Locate every Babesia divergens-infected red blood cell.
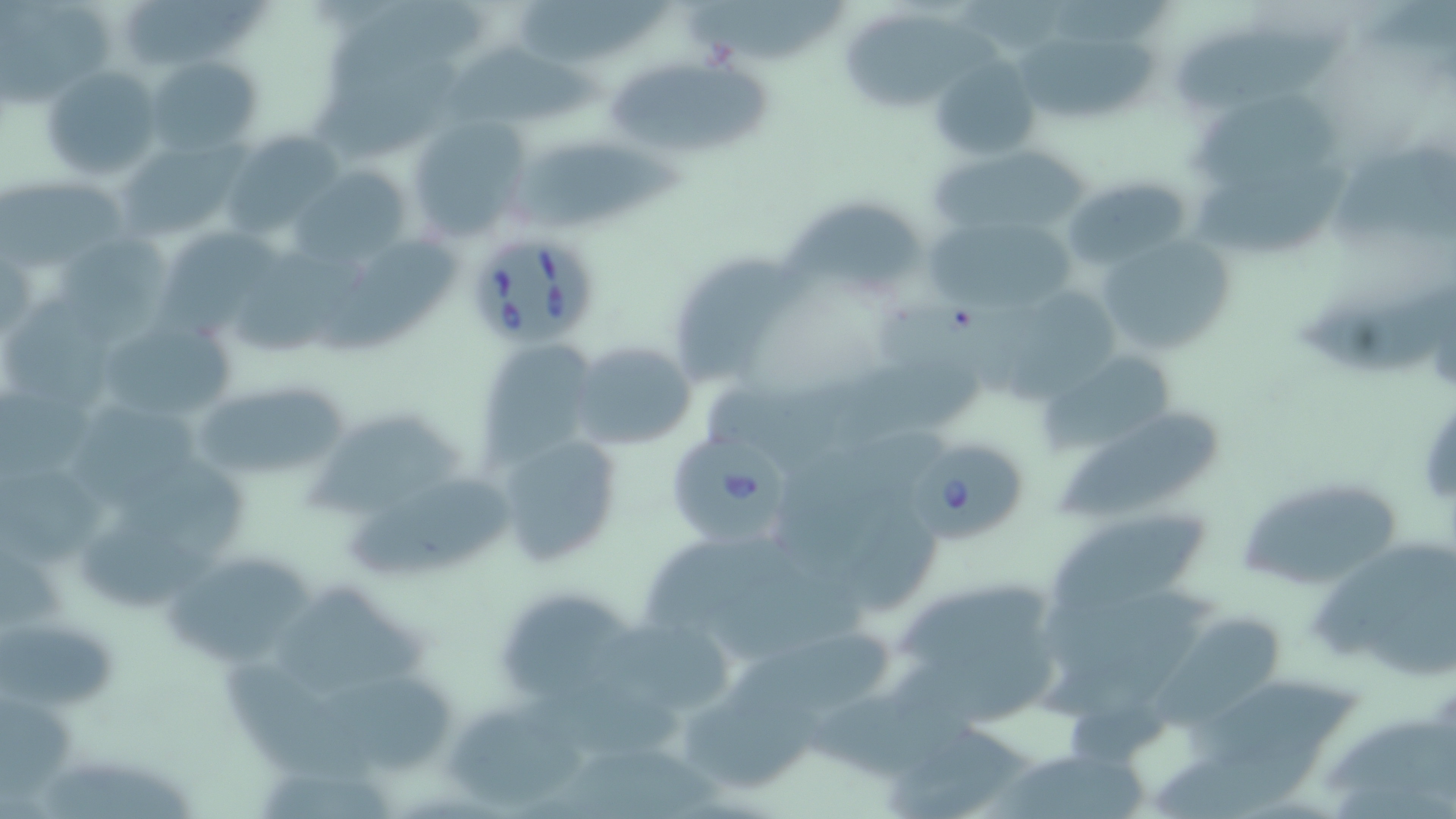
Approximate bounding boxes as named x1/y1/x2/y2 corners in pixels.
Babesia divergens-infected red blood cells: (x1=465, y1=230, x2=597, y2=346), (x1=672, y1=431, x2=793, y2=544), (x1=910, y1=436, x2=1029, y2=546).

Uninfected red blood cell locations: (x1=1, y1=0, x2=122, y2=107), (x1=129, y1=0, x2=273, y2=59), (x1=685, y1=0, x2=847, y2=72), (x1=519, y1=1, x2=672, y2=66), (x1=847, y1=13, x2=1007, y2=111), (x1=1174, y1=27, x2=1350, y2=109), (x1=1023, y1=35, x2=1161, y2=118), (x1=444, y1=45, x2=618, y2=134), (x1=312, y1=54, x2=468, y2=158), (x1=149, y1=55, x2=259, y2=156), (x1=931, y1=56, x2=1041, y2=160), (x1=605, y1=60, x2=779, y2=155), (x1=43, y1=66, x2=163, y2=182), (x1=1193, y1=92, x2=1345, y2=189), (x1=404, y1=117, x2=530, y2=243), (x1=227, y1=139, x2=344, y2=243), (x1=117, y1=141, x2=240, y2=243), (x1=508, y1=143, x2=689, y2=240), (x1=933, y1=146, x2=1088, y2=244), (x1=1337, y1=147, x2=1455, y2=241), (x1=1195, y1=166, x2=1350, y2=256), (x1=287, y1=167, x2=410, y2=269), (x1=1061, y1=174, x2=1194, y2=272), (x1=1, y1=179, x2=135, y2=268), (x1=783, y1=200, x2=932, y2=296), (x1=917, y1=220, x2=1083, y2=311), (x1=165, y1=228, x2=290, y2=331), (x1=1093, y1=231, x2=1239, y2=359), (x1=56, y1=232, x2=176, y2=339), (x1=322, y1=236, x2=461, y2=357), (x1=236, y1=246, x2=363, y2=358), (x1=674, y1=252, x2=806, y2=377), (x1=1294, y1=280, x2=1455, y2=375), (x1=881, y1=284, x2=1036, y2=402), (x1=999, y1=287, x2=1119, y2=406), (x1=1, y1=300, x2=131, y2=413), (x1=101, y1=317, x2=240, y2=427), (x1=476, y1=339, x2=598, y2=468), (x1=569, y1=341, x2=699, y2=450), (x1=1046, y1=350, x2=1180, y2=457), (x1=197, y1=385, x2=355, y2=472), (x1=78, y1=402, x2=208, y2=511), (x1=1063, y1=409, x2=1225, y2=516), (x1=303, y1=411, x2=475, y2=516), (x1=782, y1=420, x2=962, y2=568), (x1=490, y1=429, x2=623, y2=565), (x1=1, y1=468, x2=111, y2=570), (x1=114, y1=468, x2=251, y2=552), (x1=1235, y1=472, x2=1403, y2=589), (x1=343, y1=474, x2=516, y2=576), (x1=1048, y1=508, x2=1219, y2=621), (x1=79, y1=515, x2=227, y2=613), (x1=642, y1=538, x2=803, y2=633), (x1=1310, y1=545, x2=1453, y2=668), (x1=165, y1=558, x2=323, y2=669), (x1=273, y1=582, x2=437, y2=701), (x1=898, y1=583, x2=1050, y2=669), (x1=500, y1=594, x2=637, y2=696), (x1=1035, y1=611, x2=1219, y2=725), (x1=1, y1=615, x2=129, y2=716), (x1=1158, y1=615, x2=1282, y2=731), (x1=597, y1=626, x2=736, y2=713), (x1=885, y1=633, x2=1058, y2=732), (x1=724, y1=635, x2=901, y2=725), (x1=221, y1=656, x2=362, y2=779), (x1=319, y1=677, x2=453, y2=778), (x1=1186, y1=678, x2=1366, y2=770), (x1=692, y1=702, x2=822, y2=791), (x1=446, y1=710, x2=597, y2=808), (x1=1325, y1=716, x2=1456, y2=803), (x1=882, y1=728, x2=1040, y2=816), (x1=543, y1=744, x2=727, y2=819), (x1=984, y1=752, x2=1153, y2=819), (x1=261, y1=757, x2=399, y2=819), (x1=37, y1=761, x2=204, y2=819). Slide-level diagnosis: Babesia divergens. Image is 1456×819 pixels. One field of a larger specimen. Thin blood film. May-Grünwald-Giemsa stain. Optical microscopy. 1000x magnification.